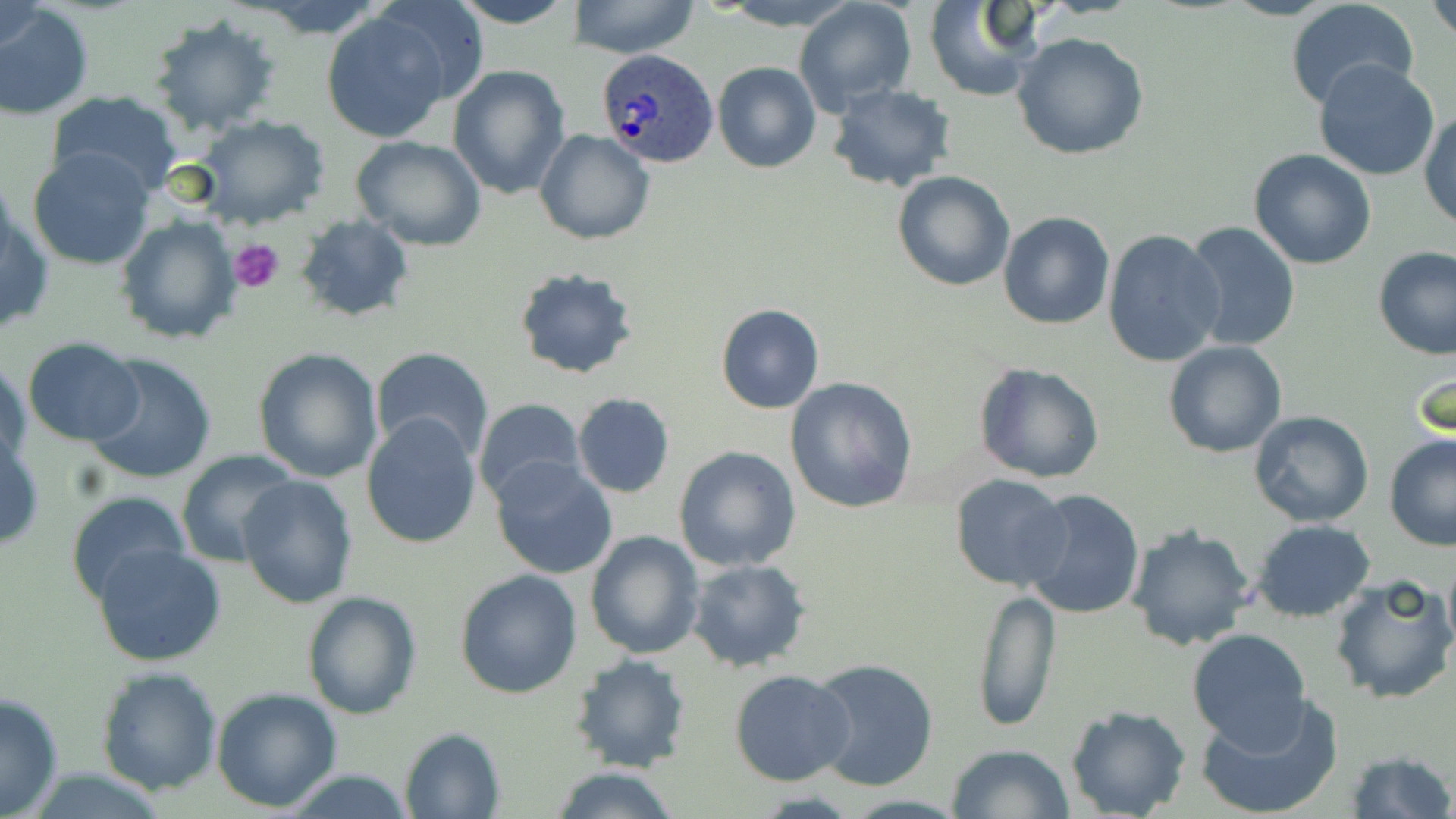 Approximate bounding boxes as (x1, y1, x2, y2) in pixels. Plasmodium ovale-infected red blood cell locations: (597, 50, 717, 169). Uninfected red blood cell locations: (371, 0, 489, 106), (449, 0, 580, 29), (570, 0, 698, 59), (715, 1, 862, 30), (793, 1, 916, 115), (923, 1, 1040, 101), (1427, 1, 1456, 38), (2, 2, 47, 57), (1287, 2, 1421, 113), (0, 3, 94, 121), (319, 11, 452, 143), (146, 15, 280, 138), (1012, 31, 1148, 159), (1314, 58, 1440, 182), (713, 61, 821, 173), (447, 64, 570, 199), (828, 84, 956, 192), (46, 89, 183, 194), (1420, 106, 1455, 231), (195, 114, 330, 228), (534, 129, 655, 244), (352, 135, 487, 250), (27, 147, 157, 271), (1248, 148, 1377, 270), (893, 172, 1016, 292), (2, 197, 52, 340), (998, 211, 1115, 329), (116, 215, 241, 344), (296, 215, 415, 322), (1184, 221, 1300, 355), (1102, 228, 1226, 369), (1374, 247, 1456, 362), (513, 267, 640, 381), (716, 304, 823, 414), (22, 338, 145, 446), (1163, 340, 1287, 458), (371, 346, 495, 464), (253, 348, 383, 483), (83, 352, 218, 486), (1, 360, 30, 474), (1409, 360, 1453, 447), (973, 362, 1104, 484), (784, 376, 918, 514), (572, 392, 675, 498), (472, 397, 586, 504), (1247, 411, 1375, 528), (361, 413, 483, 549), (0, 434, 45, 553), (1384, 435, 1456, 551), (673, 446, 801, 571), (177, 449, 300, 568), (490, 456, 619, 580), (238, 474, 357, 609), (950, 475, 1073, 590), (1018, 488, 1145, 619), (65, 490, 192, 607), (1251, 518, 1377, 622), (1127, 524, 1255, 652), (585, 529, 705, 661), (93, 544, 227, 666), (1442, 555, 1455, 660), (686, 559, 812, 673), (454, 568, 583, 699), (1328, 575, 1456, 706), (971, 586, 1061, 732), (302, 591, 420, 719), (1186, 628, 1313, 749), (568, 654, 693, 773), (807, 657, 940, 793), (95, 666, 223, 794), (729, 670, 856, 786), (212, 686, 343, 810), (0, 690, 64, 819), (1194, 694, 1343, 819), (1065, 706, 1191, 819), (399, 727, 506, 818), (947, 741, 1075, 818), (1344, 750, 1454, 819), (548, 765, 682, 819), (276, 766, 419, 819). Platelet locations: (228, 236, 285, 292). Slide-level diagnosis: Plasmodium ovale. Optical microscopy. 1000x magnification. Image is 1456×819 pixels. Single field of view. Thin blood smear. May-Grünwald-Giemsa-stained preparation.